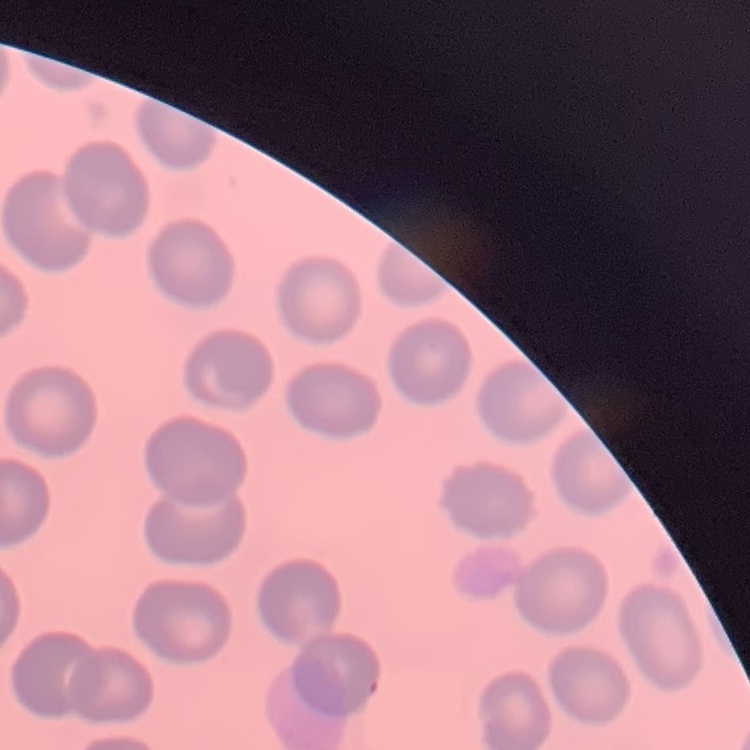
erythrocyte morphology = no rouleaux formation
preparation = thin peripheral smear
stain = Field's or Giemsa
image type = square crop of a larger photomicrograph